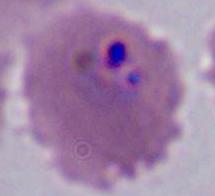
{
  "modality": "photomicrograph",
  "identification": "Plasmodium",
  "magnification": "400x or 1000x"
}